Give the position of every leukocyte.
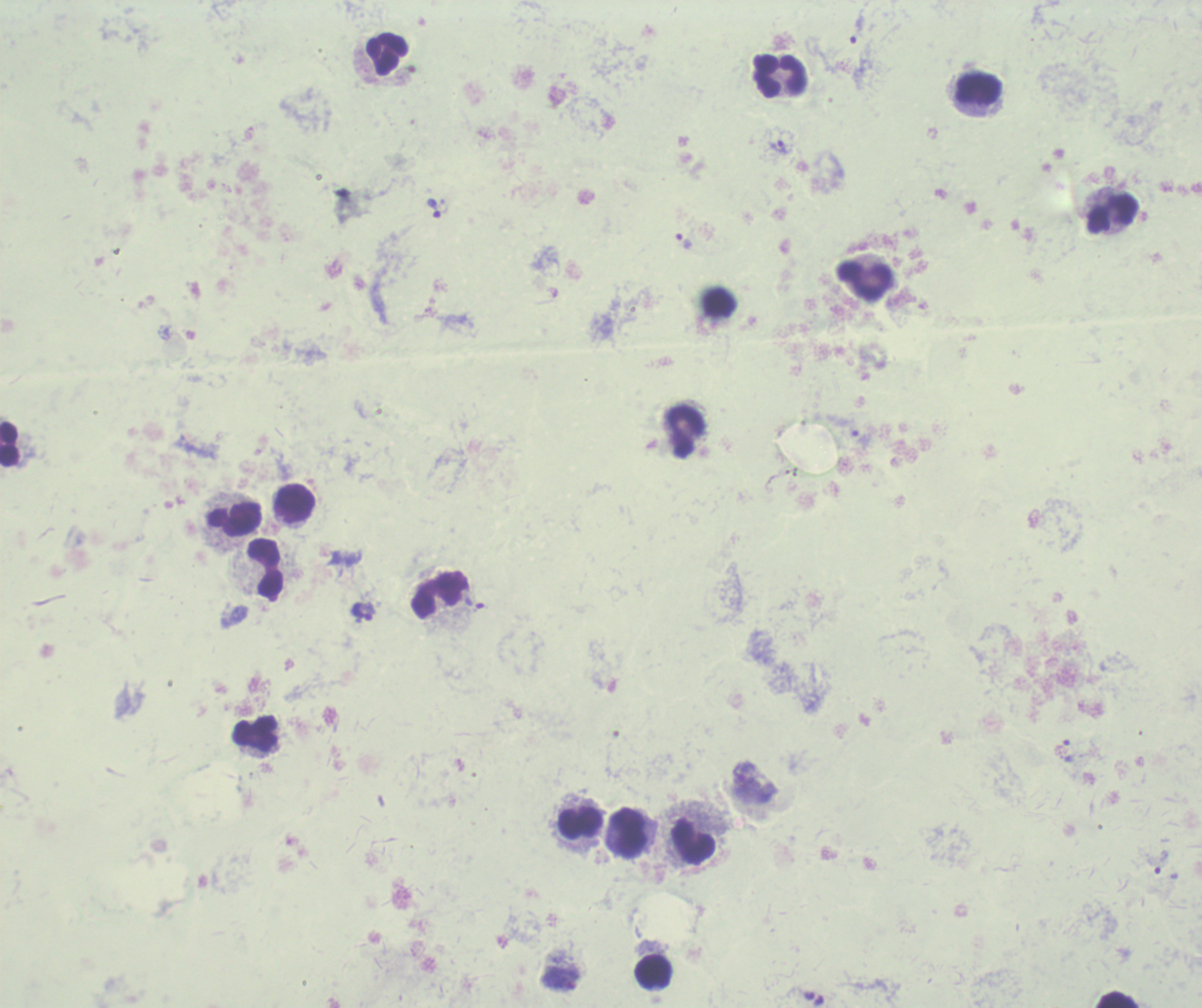
Approximate centers as [x, y] in pixels.
Leukocytes: [387, 52], [779, 76], [977, 88], [1110, 213], [867, 281], [687, 429], [10, 445], [294, 503], [234, 519], [265, 567], [438, 596], [255, 732], [580, 822], [631, 832], [693, 840], [653, 972], [1115, 999].

coordinate format = approximate centers as [x, y] in pixels
trophozoite locations = [858, 25], [777, 146], [434, 209], [684, 241], [861, 439], [363, 611], [1161, 862]
result = Plasmodium parasites identified
magnification = 100x
field of view = one from this slide
image size = 1202×1008 pixels
context = previously used in a real diagnosis
stain = Romanowsky
preparation = thick blood smear
background quality = unsatisfactory